Locate every blood parasite and identify its species.
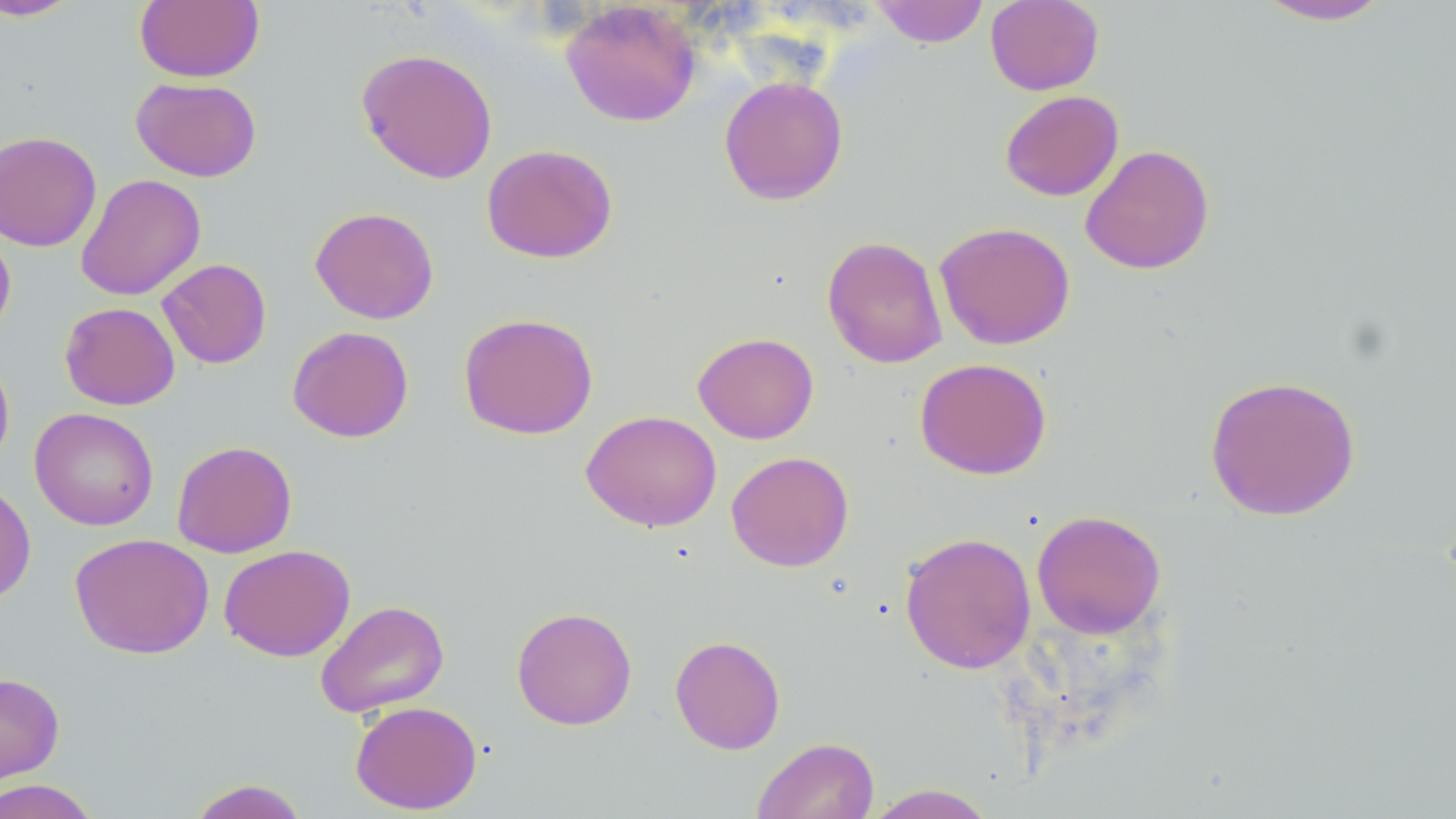
No blood parasites seen.

slide_level_diagnosis: no evidence of blood parasites
image_size: 1456×819 pixels
magnification: 1000x
preparation: thin blood film
modality: optical microscopy
stain: May-Grünwald-Giemsa
field_of_view: single
uninfected_red_blood_cell_locations: 'approximate bounding boxes as (x1, y1, x2, y2) in pixels: (134, 0, 264, 83), (985, 0, 1104, 95), (1252, 0, 1395, 26), (1, 1, 83, 22), (560, 1, 702, 127), (868, 1, 990, 47), (356, 47, 498, 184), (719, 75, 848, 205), (131, 77, 262, 182), (999, 90, 1124, 201), (0, 131, 102, 252), (481, 143, 618, 263), (1080, 144, 1215, 275), (76, 174, 206, 301), (310, 206, 439, 324), (934, 221, 1076, 350), (0, 223, 16, 340), (822, 235, 947, 369), (157, 258, 272, 369), (59, 302, 180, 410), (458, 312, 598, 439), (287, 325, 414, 443), (692, 332, 819, 444), (0, 349, 15, 472), (914, 357, 1052, 480), (1204, 374, 1361, 521), (29, 407, 159, 531), (580, 410, 722, 532), (171, 440, 297, 558), (726, 450, 854, 572), (0, 479, 37, 606), (1031, 509, 1167, 638), (899, 531, 1036, 674), (70, 533, 213, 659), (218, 544, 355, 661), (315, 599, 450, 718), (511, 606, 637, 730), (670, 634, 786, 754), (0, 671, 64, 786), (350, 701, 482, 814), (752, 736, 879, 819), (187, 778, 311, 819), (0, 779, 101, 819), (864, 784, 998, 819)'